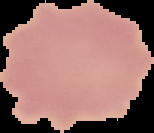

result = no malaria parasites seen
preparation = thin blood smear
image size = 154×133 pixels
image type = segmented cell region with the area outside set to black